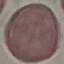

Result: no malaria parasites detected. Photographed with a smartphone camera at the microscope eyepiece. Cell patch, automatically extracted from a larger field of view and resized to 64 × 64 pixels. Giemsa-stained preparation. Thin smear of blood.